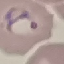

Summary:
  - Result: malaria parasites identified
  - Capture: smartphone camera at the microscope eyepiece
  - Preparation: thin blood smear
  - Stain: Giemsa
  - Image type: automatically extracted cell patch, resized to 64 × 64 pixels